Point out each leukocyte.
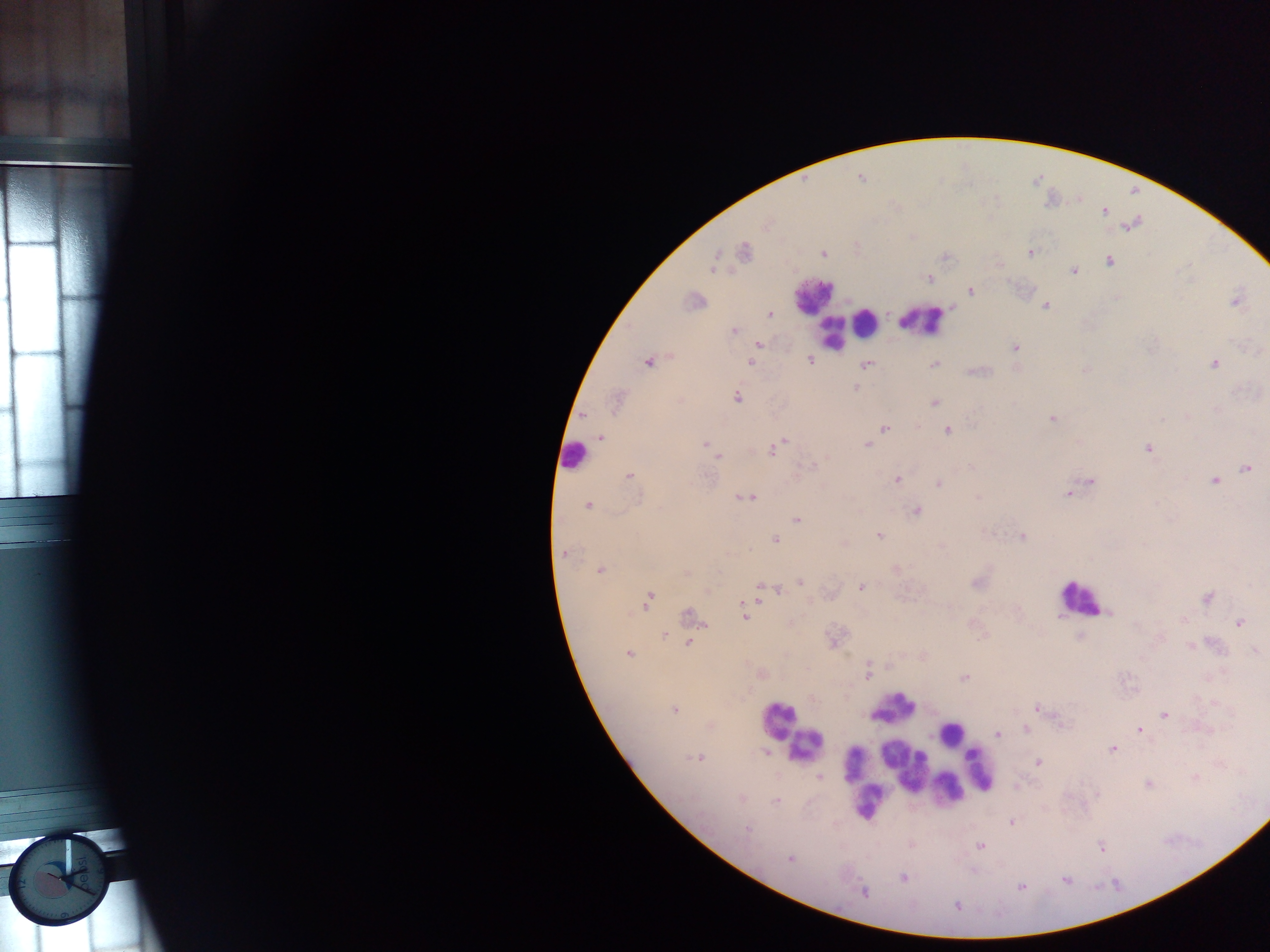

Approximate centers as (x, y) in pixels.
Leukocytes: (813, 295), (923, 320), (866, 322), (832, 334), (573, 456), (1080, 597), (893, 708), (777, 720), (950, 733), (807, 745), (854, 761), (902, 765), (979, 769), (949, 788), (866, 801).

field of view = single
country = Ghana
capture = mobile-phone photograph through a microscope
preparation = thick blood film
image size = 1270×952 pixels
Plasmodium parasite locations = approximate centers as (x, y) in pixels: (860, 178), (1105, 211), (768, 224), (1132, 225), (744, 251), (1030, 252), (824, 254), (1109, 261), (712, 268), (1074, 271), (929, 278), (970, 291), (694, 300), (1235, 301), (1045, 305), (770, 315), (734, 331), (760, 344), (1015, 348), (810, 360), (647, 363), (750, 363), (1214, 364), (866, 365), (934, 365), (855, 387), (737, 398), (616, 402), (934, 402), (1052, 418), (885, 428), (947, 430), (600, 437), (782, 442), (705, 444), (867, 445), (774, 448), (1147, 448), (718, 457), (810, 467), (971, 467), (1247, 468), (629, 476), (896, 480), (1214, 481), (1091, 482), (938, 484), (1068, 493), (747, 498), (587, 506), (917, 511), (797, 521), (879, 536), (1022, 536), (775, 539), (564, 554), (895, 569), (600, 570), (687, 572), (800, 582), (977, 583), (860, 587), (760, 588), (778, 590), (1207, 597), (648, 598), (1109, 614), (691, 615), (744, 616), (1239, 623), (663, 636), (1080, 636), (689, 642), (1190, 646), (1256, 651), (628, 653), (867, 673), (762, 674), (965, 678), (1037, 709), (675, 710), (1164, 714), (1060, 723), (1027, 729), (1138, 729), (997, 734), (1113, 749), (767, 752), (697, 758), (1038, 762), (819, 777), (1195, 777), (1147, 784), (1096, 794), (742, 799), (776, 801), (1011, 822), (746, 829), (980, 847), (1100, 847), (790, 858), (903, 878), (1065, 880), (1021, 887), (863, 892), (957, 906)